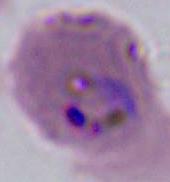
magnification = 400x or 1000x
identification = Plasmodium
modality = photomicrograph